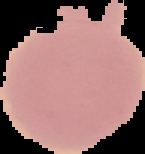
From a thin blood smear. Segmented cell region on a black background. Malaria status: uninfected. Image is 145×154 pixels.